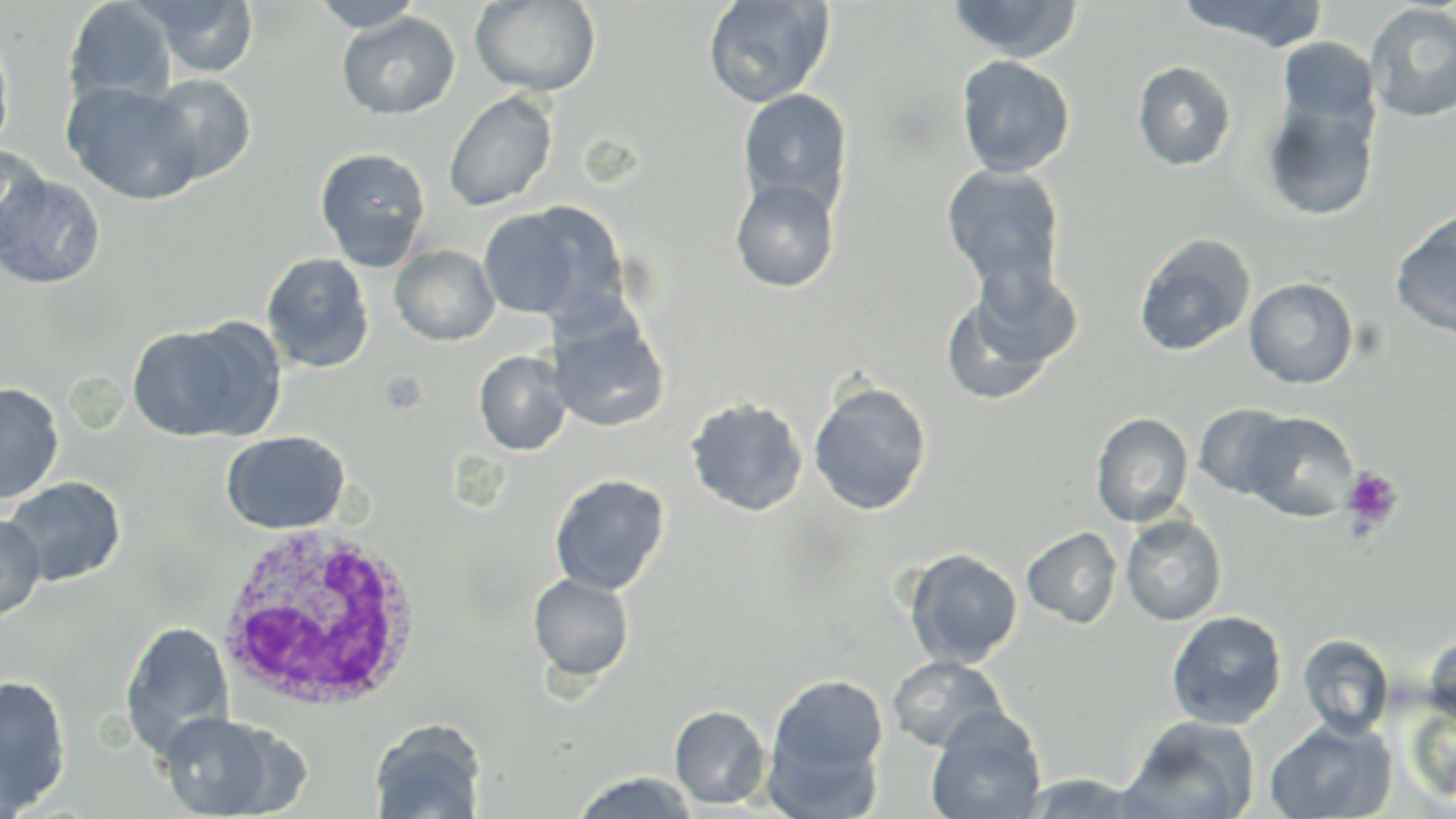
Summary:
  - Coordinate format: approximate bounding boxes as [x1, y1, x2, y2] in pixels
  - White blood cell locations: [213, 525, 426, 712]
  - Uninfected red blood cell locations: [142, 0, 260, 78], [312, 0, 424, 31], [703, 0, 835, 108], [945, 0, 1084, 62], [1174, 0, 1331, 50], [63, 1, 176, 106], [470, 1, 601, 97], [1366, 3, 1456, 122], [337, 12, 460, 120], [0, 29, 15, 159], [1278, 38, 1379, 129], [955, 55, 1075, 178], [1133, 61, 1237, 171], [145, 73, 257, 185], [62, 80, 204, 205], [737, 88, 853, 216], [444, 90, 558, 212], [1262, 92, 1380, 221], [0, 144, 50, 258], [314, 147, 432, 270], [942, 164, 1066, 293], [0, 171, 106, 290], [731, 178, 840, 293], [477, 202, 622, 323], [1390, 210, 1456, 339], [1133, 233, 1256, 357], [390, 244, 500, 346], [261, 252, 374, 373], [940, 266, 1081, 405], [1244, 277, 1359, 389], [548, 304, 671, 433], [126, 320, 279, 445], [474, 350, 570, 456], [808, 381, 931, 515], [0, 383, 64, 505], [685, 397, 808, 517], [1194, 403, 1298, 500], [1243, 411, 1358, 520], [1091, 412, 1193, 526], [220, 431, 351, 535], [549, 473, 670, 595], [1, 476, 126, 588], [0, 512, 46, 622], [1121, 515, 1227, 625], [1022, 527, 1122, 628], [903, 548, 1023, 668], [528, 572, 635, 683], [1166, 610, 1287, 730], [120, 621, 236, 758], [1423, 630, 1456, 724], [1298, 634, 1394, 738], [887, 655, 1008, 752], [766, 673, 888, 792], [0, 674, 72, 813], [669, 705, 771, 809], [925, 709, 1046, 819], [155, 710, 298, 818], [1123, 714, 1261, 818], [1264, 719, 1396, 818], [369, 720, 487, 818], [1018, 770, 1151, 817], [568, 771, 700, 818]
  - Platelet locations: [1340, 465, 1404, 534]
  - Slide-level diagnosis: Plasmodium ovale
  - Preparation: thin blood film
  - Image size: 1456×819 pixels
  - Magnification: 1000x
  - Stain: May-Grünwald-Giemsa
  - Modality: light microscopy
  - Field of view: single